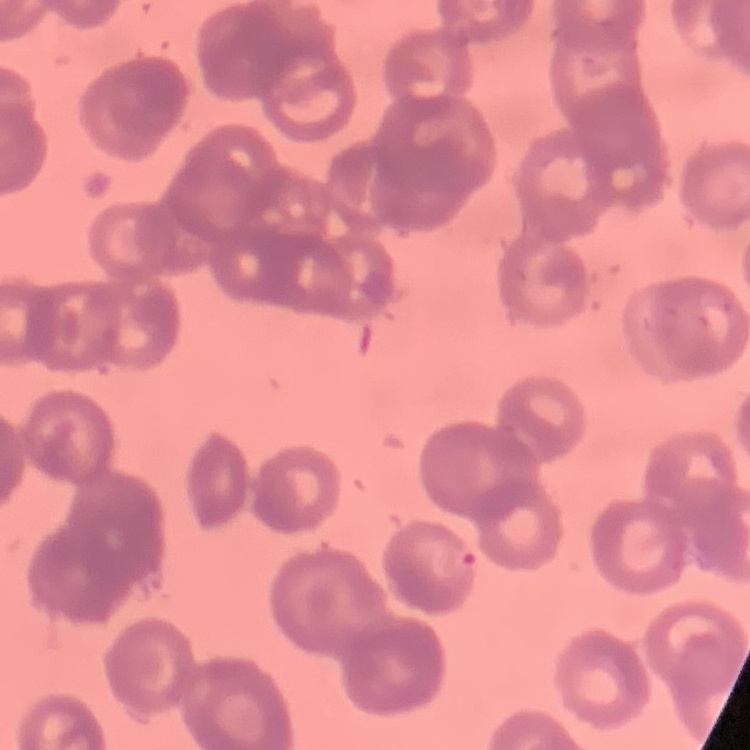

{
  "erythrocyte_morphology": "rouleaux formation",
  "stain": "Field's or Giemsa",
  "image_type": "square crop of a larger photomicrograph",
  "preparation": "thin peripheral smear"
}